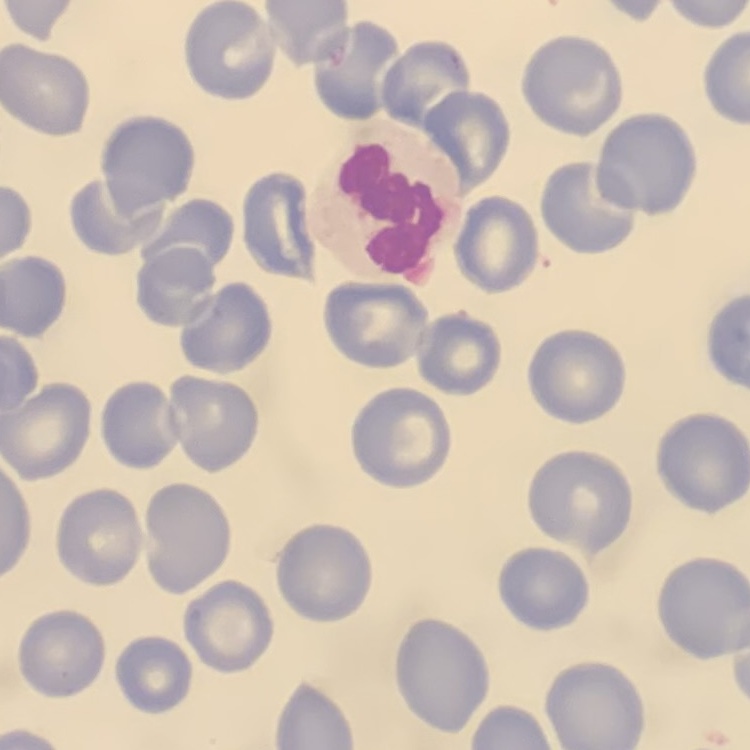 The erythrocytes show no rouleaux formation. Stained with either Field's or Giemsa. Thin blood film. Square crop of a larger photomicrograph.